Classify this cell by malaria status.
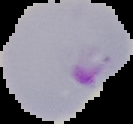
Parasitized.

image type = segmented cell region on a black background
image size = 133×124 pixels
preparation = thin blood film